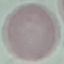
Malaria status: uninfected. Giemsa stain. Cell patch, automatically extracted from a larger field of view and resized to 64 × 64 pixels. Thin blood smear. Acquired by smartphone through the microscope eyepiece.